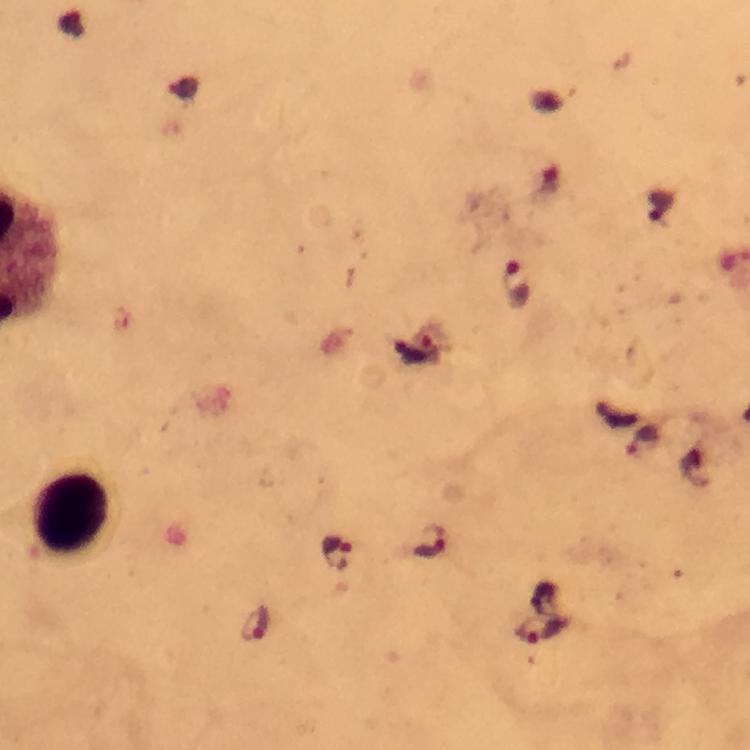
Approximate centers as (x, y) in pixels.
Summary:
  - Leukocyte locations: (73, 513)
  - Plasmodium parasite locations: (517, 286), (418, 347), (644, 441), (431, 544), (339, 553), (255, 623), (544, 630)
  - Magnification: 100x
  - Context: from a diagnostic examination for malaria
  - Capture: smartphone camera through the microscope
  - Image size: 750×750 pixels
  - Cropped from: one field of view
  - Immersion oil: used
  - Preparation: thick smear
  - Stain: Giemsa